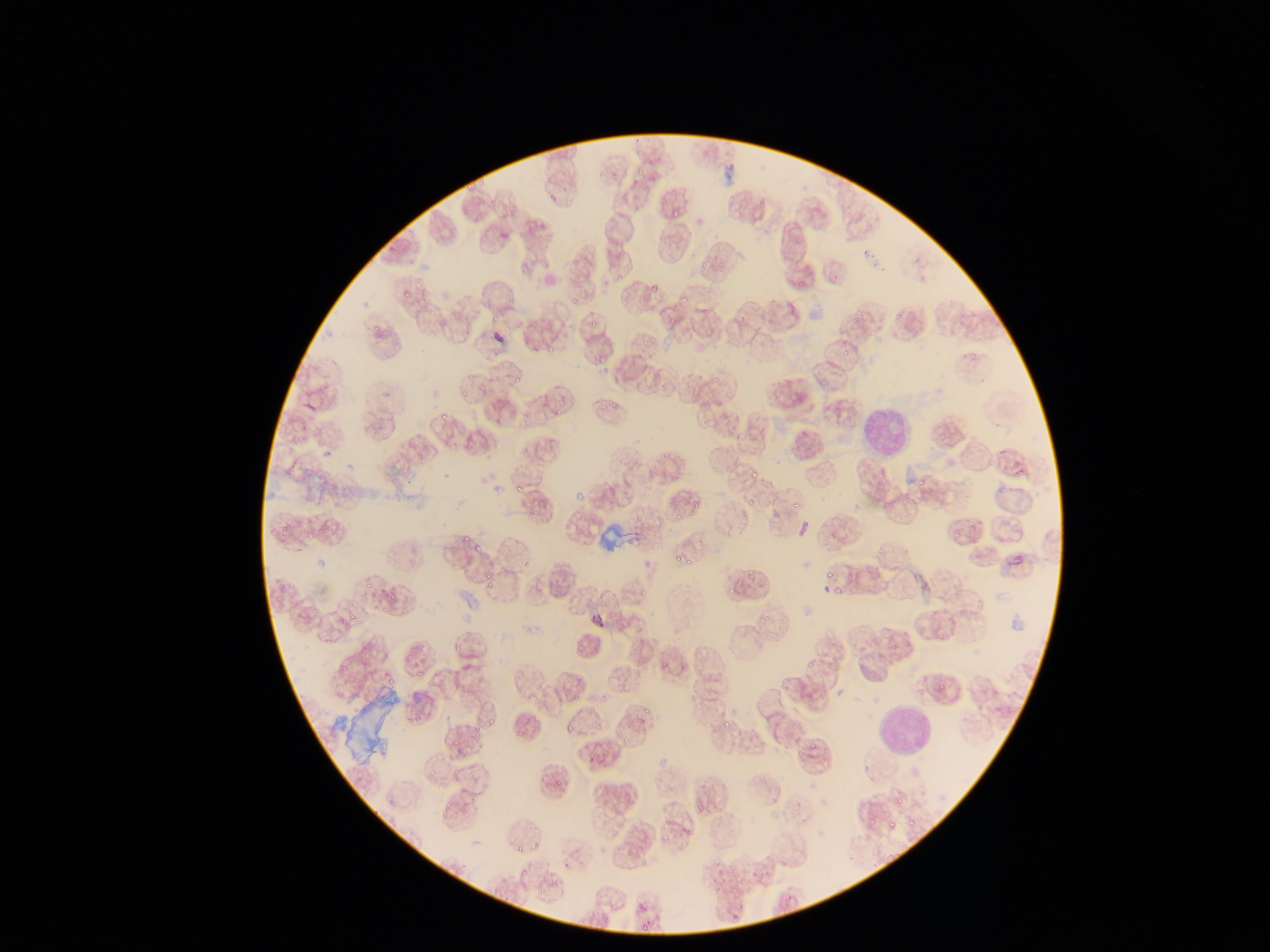
Approximate bounding boxes as {left, top, right, bottom} in pixels.
Summary:
  - Artifact (stain precipitate or debris) locations: {599, 516, 632, 566}, {342, 689, 402, 765}
  - Plasmodium parasite locations: {566, 142, 580, 155}, {636, 166, 645, 176}, {465, 178, 476, 191}, {725, 192, 738, 206}, {549, 194, 559, 205}, {465, 206, 473, 214}, {671, 210, 684, 222}, {858, 218, 874, 234}, {538, 220, 548, 228}, {500, 232, 509, 241}, {615, 247, 628, 256}, {696, 258, 710, 274}, {616, 268, 626, 280}, {795, 271, 808, 287}, {568, 274, 581, 286}, {412, 280, 425, 290}, {647, 284, 657, 294}, {403, 292, 414, 302}, {501, 293, 515, 303}, {679, 294, 689, 306}, {570, 295, 581, 304}, {769, 295, 779, 308}, {748, 299, 757, 310}, {891, 305, 903, 321}, {491, 310, 502, 327}, {855, 310, 865, 323}, {591, 311, 603, 328}, {666, 313, 679, 328}, {373, 320, 381, 329}, {543, 321, 552, 330}, {697, 326, 709, 341}, {643, 330, 666, 345}, {372, 335, 382, 346}, {839, 340, 853, 357}, {546, 342, 556, 352}, {592, 345, 606, 366}, {967, 347, 979, 361}, {710, 368, 724, 383}, {514, 370, 525, 391}, {464, 371, 476, 382}, {817, 373, 833, 385}, {460, 384, 470, 399}, {723, 390, 731, 401}, {557, 397, 564, 405}, {596, 399, 607, 412}, {552, 401, 565, 416}, {609, 401, 622, 418}, {702, 401, 713, 410}, {439, 410, 449, 422}, {371, 416, 384, 435}, {943, 419, 955, 432}, {444, 439, 454, 451}, {658, 448, 668, 462}, {674, 450, 684, 460}, {397, 456, 416, 473}, {710, 463, 721, 475}, {286, 467, 296, 478}, {751, 469, 761, 483}, {646, 472, 657, 485}, {504, 474, 519, 482}, {916, 475, 931, 488}, {762, 481, 773, 494}, {327, 482, 341, 497}, {513, 482, 524, 493}, {305, 490, 312, 501}, {906, 493, 921, 507}, {747, 495, 757, 512}, {788, 501, 800, 512}, {684, 502, 702, 513}, {635, 506, 646, 526}, {673, 509, 686, 526}, {772, 509, 780, 518}, {525, 512, 535, 523}, {965, 513, 985, 530}, {281, 521, 291, 535}, {319, 521, 330, 534}, {954, 522, 966, 539}, {829, 531, 838, 542}, {462, 533, 473, 544}, {876, 542, 887, 556}, {473, 544, 484, 555}, {676, 555, 686, 563}, {550, 556, 563, 575}, {682, 557, 694, 565}, {523, 560, 530, 568}, {499, 566, 509, 580}, {847, 567, 859, 589}, {744, 569, 756, 582}, {477, 571, 495, 588}, {363, 577, 374, 590}, {279, 578, 295, 594}, {637, 579, 647, 601}, {727, 584, 738, 596}, {830, 584, 841, 596}, {389, 591, 398, 600}, {599, 597, 607, 614}, {311, 602, 319, 613}, {398, 602, 406, 617}, {286, 603, 295, 614}, {611, 603, 624, 610}, {348, 611, 359, 626}, {759, 613, 769, 625}, {737, 626, 749, 638}, {939, 628, 949, 642}, {464, 630, 474, 636}, {324, 635, 332, 646}, {890, 639, 897, 657}, {588, 643, 603, 653}, {455, 644, 466, 653}, {573, 647, 584, 663}, {654, 653, 673, 670}, {416, 654, 427, 666}, {805, 657, 816, 668}, {339, 661, 345, 670}, {562, 665, 573, 676}, {415, 666, 426, 678}, {781, 670, 790, 691}, {387, 674, 395, 685}, {342, 676, 357, 690}, {939, 682, 949, 693}, {712, 684, 726, 695}, {569, 687, 583, 699}, {804, 687, 815, 700}, {591, 700, 600, 714}, {643, 704, 651, 714}, {716, 707, 733, 725}, {414, 712, 422, 723}, {487, 714, 499, 728}, {632, 715, 645, 725}, {565, 716, 577, 733}, {407, 718, 415, 725}, {721, 720, 732, 731}, {648, 722, 659, 729}, {593, 725, 605, 736}, {515, 726, 526, 740}, {469, 727, 477, 737}, {624, 732, 632, 741}, {453, 736, 463, 748}, {473, 740, 481, 747}, {810, 740, 821, 747}, {797, 746, 806, 757}, {585, 747, 597, 765}, {806, 751, 818, 761}, {468, 761, 480, 774}, {864, 764, 873, 773}, {759, 777, 769, 788}, {556, 778, 562, 787}, {479, 783, 490, 791}, {702, 783, 710, 794}, {775, 786, 785, 792}, {475, 793, 481, 804}, {704, 797, 715, 809}, {896, 798, 905, 808}, {608, 799, 623, 819}, {438, 804, 449, 815}, {866, 810, 878, 824}, {907, 815, 918, 830}, {887, 819, 896, 831}, {680, 827, 694, 843}, {658, 830, 668, 844}, {527, 834, 540, 851}, {517, 845, 523, 855}, {562, 859, 571, 869}, {451, 864, 462, 878}, {519, 866, 531, 878}, {761, 866, 774, 883}, {544, 870, 558, 887}, {710, 872, 729, 894}, {536, 890, 545, 901}, {784, 894, 791, 905}, {637, 903, 646, 912}, {725, 914, 737, 923}, {640, 920, 649, 930} | approximate {x, y} pixel centers of objects too small to bound: {319, 440}, {907, 513}, {309, 535}, {829, 573}, {643, 667}, {540, 779}
  - Leukocyte locations: {853, 401, 913, 452}, {876, 694, 929, 758}
  - Capture: mobile-phone photograph through a microscope
  - Preparation: thin blood film
  - Field of view: single
  - Image size: 1270×952 pixels
  - Country: Ghana